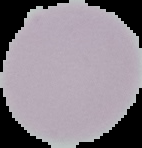
Summary:
  - Result: no malaria parasites seen
  - Image type: cell region segmented out of the field of view; surrounding area masked to black
  - Image size: 142×148 pixels
  - Preparation: thin blood film